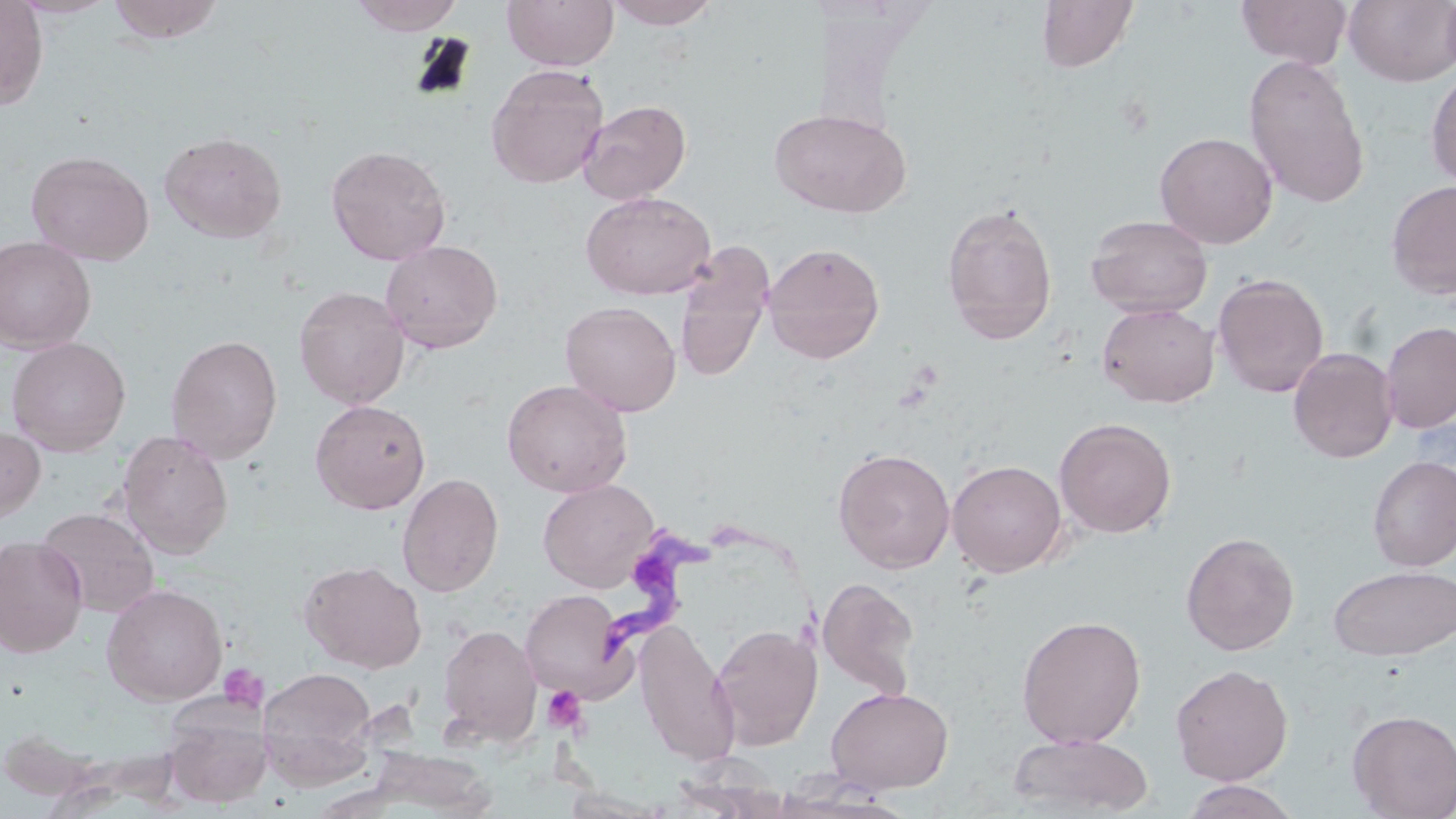
slide-level diagnosis = Trypanosoma brucei
modality = light microscopy
platelet locations = approximate bounding boxes as named x1/y1/x2/y2 corners in pixels: (x1=218, y1=664, x2=266, y2=711), (x1=542, y1=685, x2=587, y2=733)
image size = 1456×819 pixels
Trypanosoma brucei locations = approximate bounding boxes as named x1/y1/x2/y2 corners in pixels: (x1=595, y1=528, x2=824, y2=659)
field of view = one of a larger specimen
preparation = thin blood film
stain = May-Grünwald-Giemsa
magnification = 1000x
uninfected red blood cell locations = approximate bounding boxes as named x1/y1/x2/y2 corners in pixels: (x1=0, y1=0, x2=49, y2=110), (x1=7, y1=0, x2=119, y2=19), (x1=105, y1=0, x2=224, y2=44), (x1=350, y1=0, x2=465, y2=35), (x1=502, y1=0, x2=618, y2=71), (x1=605, y1=0, x2=719, y2=29), (x1=1036, y1=0, x2=1139, y2=73), (x1=1236, y1=0, x2=1352, y2=68), (x1=1344, y1=0, x2=1455, y2=86), (x1=1439, y1=0, x2=1456, y2=81), (x1=1242, y1=53, x2=1370, y2=209), (x1=486, y1=63, x2=609, y2=189), (x1=1425, y1=65, x2=1456, y2=191), (x1=577, y1=99, x2=692, y2=204), (x1=769, y1=109, x2=913, y2=218), (x1=158, y1=130, x2=287, y2=244), (x1=1155, y1=131, x2=1278, y2=248), (x1=325, y1=144, x2=451, y2=265), (x1=25, y1=150, x2=154, y2=265), (x1=1386, y1=180, x2=1456, y2=300), (x1=581, y1=191, x2=716, y2=301), (x1=941, y1=203, x2=1058, y2=345), (x1=1086, y1=214, x2=1212, y2=318), (x1=0, y1=236, x2=97, y2=353), (x1=380, y1=239, x2=503, y2=354), (x1=673, y1=240, x2=774, y2=384), (x1=762, y1=242, x2=885, y2=364), (x1=1213, y1=272, x2=1329, y2=398), (x1=294, y1=286, x2=409, y2=409), (x1=560, y1=300, x2=682, y2=416), (x1=1097, y1=302, x2=1219, y2=407), (x1=1380, y1=322, x2=1456, y2=433), (x1=166, y1=333, x2=283, y2=464), (x1=6, y1=336, x2=131, y2=456), (x1=1287, y1=346, x2=1399, y2=463), (x1=501, y1=379, x2=632, y2=497), (x1=309, y1=399, x2=431, y2=514), (x1=1054, y1=417, x2=1177, y2=538), (x1=0, y1=425, x2=45, y2=524), (x1=116, y1=430, x2=234, y2=560), (x1=832, y1=447, x2=956, y2=574), (x1=1368, y1=456, x2=1456, y2=572), (x1=947, y1=459, x2=1067, y2=577), (x1=397, y1=473, x2=504, y2=597), (x1=538, y1=479, x2=659, y2=592), (x1=35, y1=507, x2=160, y2=618), (x1=1180, y1=532, x2=1300, y2=656), (x1=0, y1=535, x2=88, y2=657), (x1=299, y1=560, x2=427, y2=673), (x1=1329, y1=565, x2=1456, y2=661), (x1=817, y1=576, x2=920, y2=699), (x1=101, y1=584, x2=228, y2=705), (x1=519, y1=589, x2=635, y2=703), (x1=1016, y1=614, x2=1147, y2=749), (x1=634, y1=622, x2=740, y2=768), (x1=710, y1=622, x2=823, y2=750), (x1=437, y1=623, x2=542, y2=747), (x1=1171, y1=663, x2=1294, y2=785), (x1=258, y1=667, x2=378, y2=787), (x1=826, y1=686, x2=953, y2=793), (x1=164, y1=707, x2=271, y2=808), (x1=1347, y1=709, x2=1456, y2=819), (x1=1007, y1=732, x2=1155, y2=817), (x1=363, y1=748, x2=499, y2=815), (x1=1179, y1=779, x2=1302, y2=819)